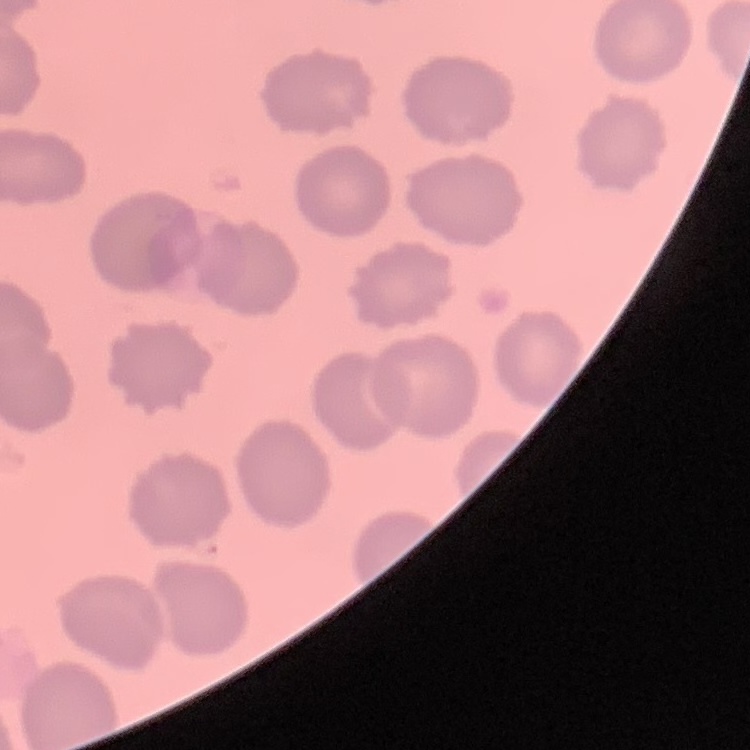

{
  "red_blood_cell_morphology": "no rouleaux formation",
  "preparation": "thin blood film",
  "stain": "Field's or Giemsa",
  "image_type": "one tile cut from a larger photomicrograph"
}